Locate every blood parasite and identify its species.
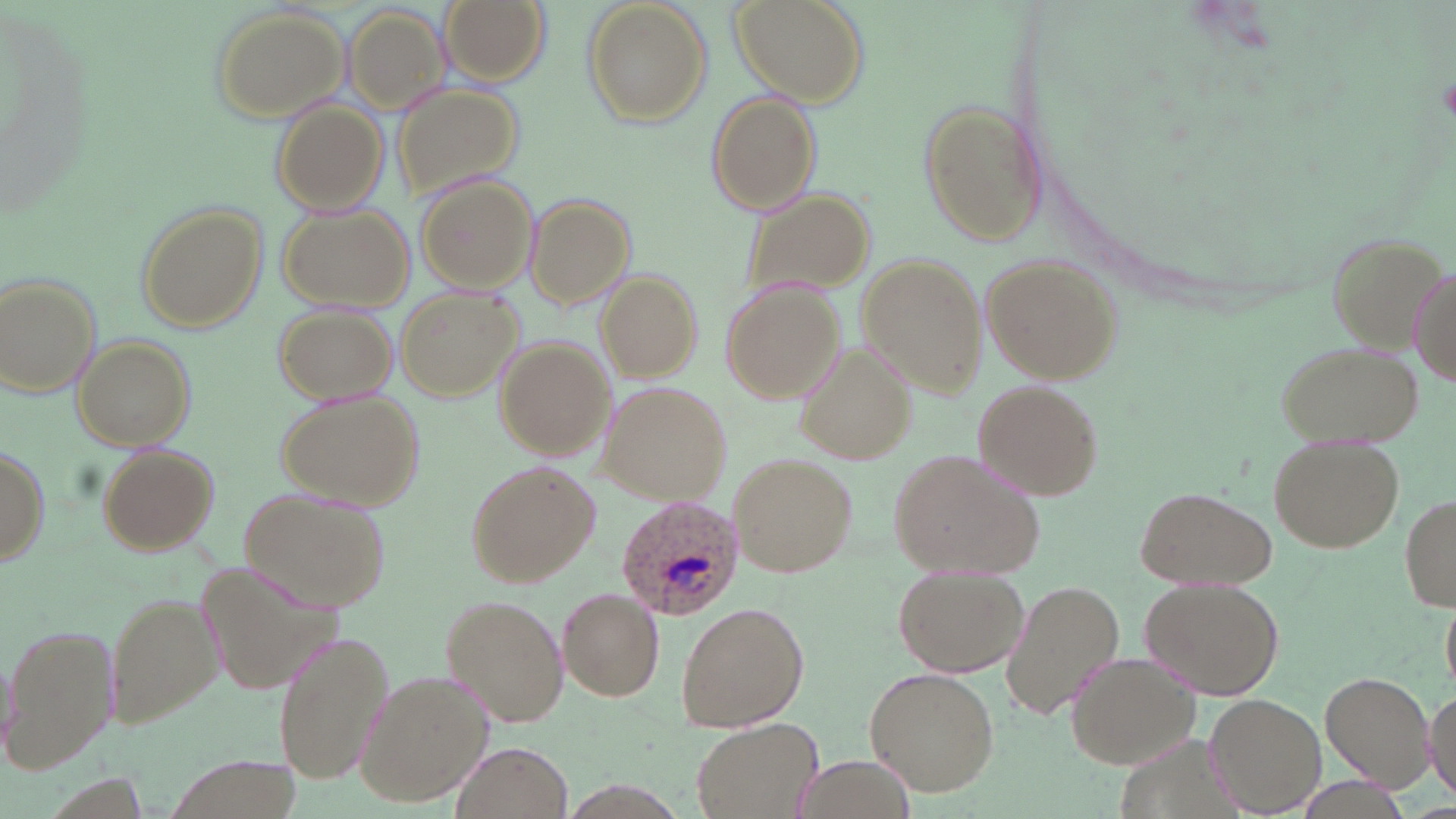

Approximate bounding boxes as [x1, y1, x2, y2] in pixels.
Plasmodium ovale-infected red blood cells: [615, 496, 742, 619].
No Plasmodium falciparum, Plasmodium malariae, Plasmodium vivax, Babesia divergens, or Trypanosoma brucei observed.

Uninfected red blood cell locations: [437, 0, 549, 88], [584, 0, 712, 127], [728, 0, 867, 107], [211, 5, 352, 121], [345, 6, 454, 110], [395, 86, 526, 202], [705, 92, 823, 215], [919, 96, 1047, 249], [271, 100, 388, 215], [416, 176, 541, 293], [739, 186, 878, 308], [522, 193, 635, 311], [134, 202, 267, 335], [276, 205, 412, 310], [1325, 228, 1446, 346], [981, 252, 1122, 386], [856, 253, 990, 397], [1409, 262, 1455, 392], [595, 269, 701, 382], [0, 272, 101, 401], [722, 281, 842, 404], [397, 287, 523, 401], [274, 304, 399, 404], [73, 335, 195, 450], [496, 338, 617, 460], [1277, 339, 1423, 448], [799, 341, 915, 465], [976, 379, 1102, 498], [600, 382, 732, 504], [278, 390, 424, 511], [1270, 437, 1402, 551], [95, 442, 220, 555], [0, 445, 49, 566], [888, 448, 1042, 576], [730, 452, 858, 576], [464, 459, 601, 588], [1138, 486, 1274, 590], [240, 489, 391, 613], [1401, 492, 1456, 613], [892, 565, 1028, 678], [1142, 573, 1284, 698], [1002, 580, 1124, 719], [557, 586, 663, 702], [106, 589, 222, 729], [439, 594, 570, 727], [675, 600, 807, 733], [1443, 601, 1455, 690], [4, 623, 117, 775], [272, 630, 393, 788], [1064, 650, 1203, 769], [867, 665, 1000, 794], [355, 669, 493, 809], [1321, 674, 1433, 786], [1424, 685, 1456, 805], [1206, 692, 1328, 816], [691, 718, 823, 819], [453, 742, 573, 819], [791, 753, 918, 819]. Slide-level diagnosis: Plasmodium ovale. Light microscopy. Image is 1456×819 pixels. Thin blood smear. Single field of view. May-Grünwald-Giemsa stain. 1000x magnification.